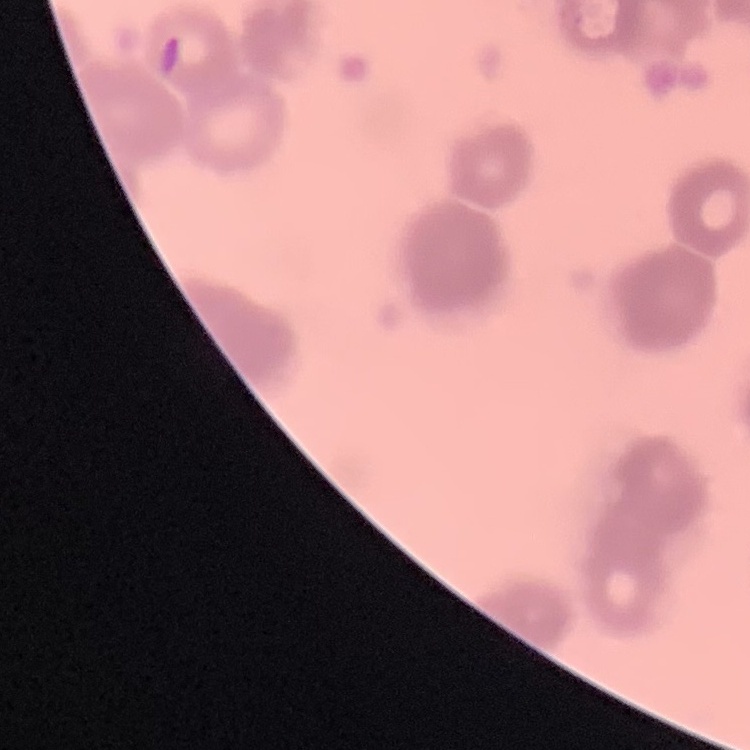

erythrocyte morphology = rouleaux formation
image type = one tile cut from a larger photomicrograph
stain = Field's or Giemsa
preparation = thin blood smear